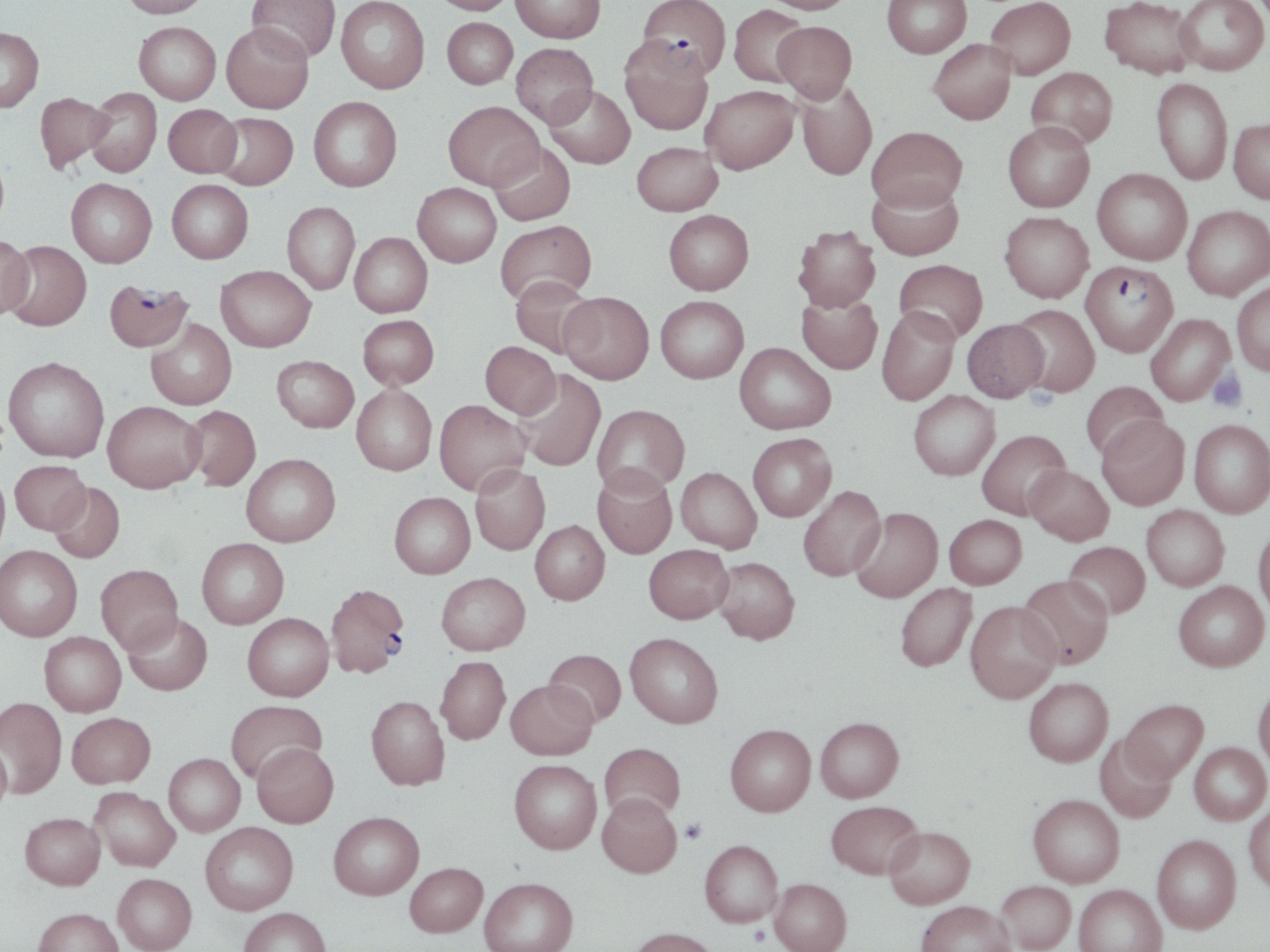

Approximate bounding boxes as (x1, y1, x2, y2) in pixels. Plasmodium falciparum-infected red blood cell locations: (637, 0, 731, 77), (1081, 260, 1179, 357), (103, 278, 194, 352), (325, 583, 410, 677). Uninfected red blood cell locations: (119, 0, 211, 18), (248, 0, 341, 63), (336, 0, 429, 93), (428, 0, 517, 15), (511, 0, 605, 43), (761, 0, 857, 14), (882, 0, 971, 59), (985, 0, 1076, 79), (1099, 0, 1199, 79), (1174, 0, 1269, 75), (728, 5, 809, 88), (442, 17, 517, 88), (773, 21, 857, 102), (134, 22, 221, 104), (221, 22, 314, 113), (0, 27, 44, 111), (620, 37, 714, 135), (928, 38, 1016, 124), (511, 43, 598, 127), (1026, 67, 1117, 149), (1151, 78, 1232, 186), (796, 81, 877, 181), (545, 85, 635, 169), (700, 86, 799, 174), (86, 88, 162, 177), (34, 92, 113, 173), (308, 96, 402, 192), (444, 101, 543, 190), (163, 104, 242, 177), (212, 112, 298, 190), (1229, 118, 1270, 203), (1002, 122, 1094, 212), (867, 126, 967, 212), (488, 141, 576, 226), (631, 142, 723, 216), (1092, 168, 1192, 265), (66, 178, 157, 267), (167, 179, 253, 263), (867, 179, 964, 261), (412, 183, 501, 267), (282, 201, 360, 295), (1182, 205, 1270, 300), (664, 209, 754, 295), (999, 212, 1094, 302), (495, 220, 596, 305), (792, 225, 881, 312), (350, 233, 432, 317), (0, 235, 35, 319), (3, 241, 92, 330), (894, 259, 988, 343), (216, 265, 315, 351), (510, 274, 597, 358), (1232, 281, 1270, 376), (796, 291, 883, 374), (559, 292, 654, 384), (655, 295, 749, 383), (1010, 304, 1100, 397), (876, 307, 960, 405), (1146, 313, 1235, 405), (358, 314, 439, 388), (962, 318, 1048, 402), (146, 319, 236, 409), (480, 341, 561, 419), (735, 342, 836, 434), (272, 355, 359, 432), (3, 356, 110, 462), (512, 369, 605, 471), (1081, 381, 1168, 462), (352, 384, 437, 475), (908, 390, 1000, 480), (434, 399, 530, 495), (103, 401, 205, 492), (592, 404, 689, 494), (183, 405, 261, 491), (1097, 416, 1190, 510), (1189, 419, 1270, 518), (976, 429, 1071, 519), (747, 433, 836, 521), (241, 453, 340, 547), (10, 460, 90, 535), (470, 465, 550, 555), (592, 465, 677, 559), (1025, 465, 1114, 545), (676, 467, 761, 552), (0, 470, 10, 560), (48, 482, 125, 564), (798, 485, 886, 581), (389, 492, 475, 579), (1141, 505, 1229, 591), (849, 507, 942, 602), (944, 514, 1026, 589), (530, 520, 609, 604), (1253, 522, 1270, 616), (197, 538, 289, 628), (1064, 541, 1150, 619), (644, 544, 733, 623), (0, 545, 82, 641), (712, 557, 799, 644), (96, 564, 183, 654), (436, 572, 530, 655), (1017, 574, 1114, 669), (1173, 581, 1269, 672), (895, 583, 977, 671), (966, 601, 1060, 703), (124, 613, 212, 695), (243, 613, 334, 700), (40, 631, 126, 716), (625, 632, 723, 728), (543, 649, 626, 726), (435, 656, 510, 745), (1023, 677, 1113, 766), (506, 679, 597, 759), (1253, 682, 1270, 771), (366, 695, 449, 790), (0, 697, 66, 798), (1121, 699, 1208, 782), (226, 700, 327, 782), (66, 712, 155, 788), (815, 716, 903, 802), (725, 724, 816, 816), (1094, 734, 1177, 823), (1, 737, 12, 820), (252, 742, 338, 827), (1189, 742, 1269, 825), (599, 743, 685, 821), (163, 753, 245, 836), (509, 759, 601, 854), (89, 787, 180, 871), (597, 792, 681, 877), (1028, 794, 1124, 887), (826, 800, 924, 879), (1244, 803, 1270, 894), (20, 812, 105, 889), (328, 812, 424, 900), (200, 822, 298, 915), (884, 826, 975, 909), (1152, 834, 1241, 933), (700, 839, 783, 927), (404, 862, 487, 937), (113, 873, 196, 952), (479, 877, 578, 952), (769, 878, 851, 952), (996, 880, 1076, 951), (1073, 884, 1167, 952), (916, 900, 1015, 952), (33, 907, 123, 952), (239, 907, 331, 952), (627, 927, 719, 952). Platelet locations: (1208, 367, 1248, 412), (680, 818, 706, 843), (750, 925, 769, 946). Slide-level diagnosis: Plasmodium falciparum. Optical microscopy. May-Grünwald-Giemsa-stained preparation. Image is 1270×952 pixels. One field of a larger specimen. Thin blood smear. 1000x magnification.